Outline Plasmodium malariae parasites and classify them by life-cycle stage.
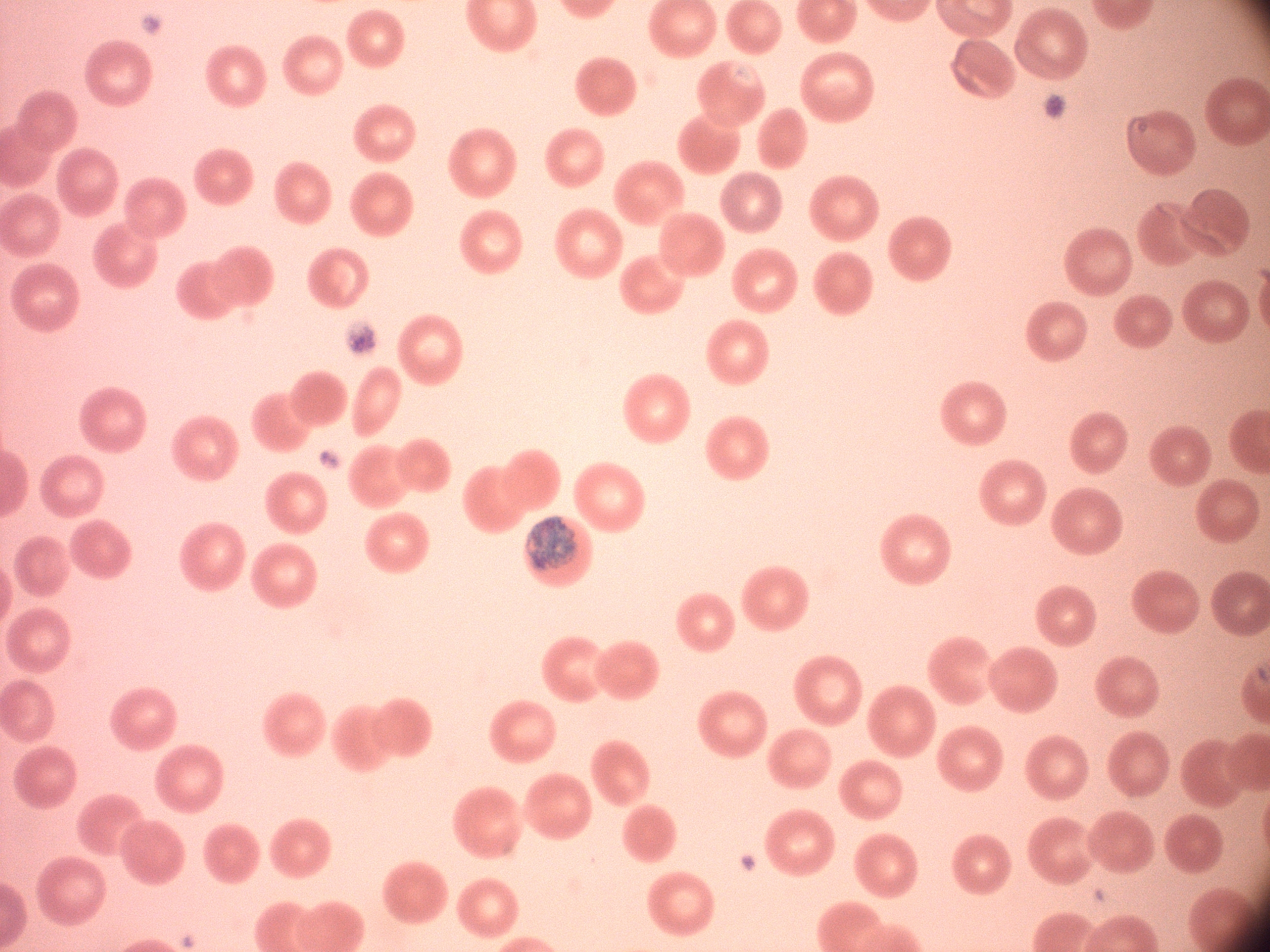
Approximate bounding boxes as named x1/y1/x2/y2 corners in pixels, from the source annotation, which is not necessarily exhaustive.
Schizonts: (x1=530, y1=517, x2=578, y2=571).

species = Plasmodium malariae
microscope = Leica DM2000 with built-in camera
stain = Giemsa
field of view = one from this slide
preparation = thin blood film
magnification = 100x
image size = 1270×952 pixels